Identify the blood parasite species.
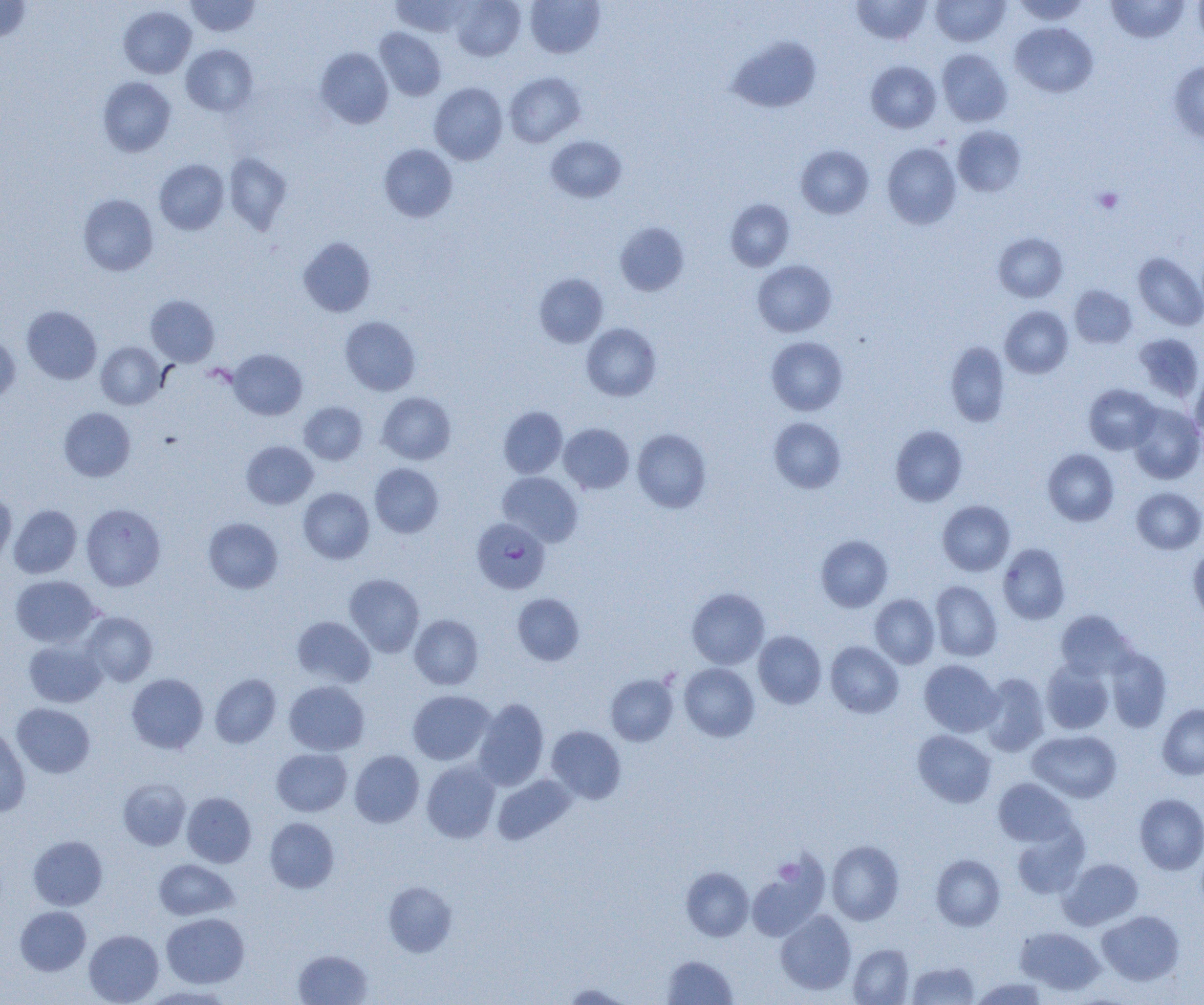
Plasmodium falciparum.

Summary:
  - Coordinate format: approximate bounding boxes as [x1, y1, x2, y2] in pixels
  - Platelet locations: [1093, 187, 1123, 213], [774, 858, 799, 883]
  - Uninfected red blood cell locations: [0, 0, 31, 43], [186, 0, 260, 37], [389, 0, 471, 36], [451, 0, 525, 60], [525, 0, 605, 58], [851, 0, 931, 45], [931, 0, 1009, 46], [1012, 0, 1091, 24], [1106, 0, 1190, 43], [1193, 0, 1204, 49], [119, 6, 196, 78], [1011, 22, 1098, 97], [375, 27, 447, 100], [728, 35, 821, 114], [181, 44, 258, 116], [315, 47, 394, 128], [937, 49, 1012, 126], [1168, 60, 1204, 144], [866, 61, 941, 133], [504, 72, 585, 147], [98, 77, 176, 157], [429, 83, 508, 165], [953, 125, 1026, 197], [545, 135, 626, 203], [882, 143, 961, 229], [379, 144, 458, 222], [795, 145, 874, 218], [224, 152, 292, 234], [154, 159, 229, 235], [78, 194, 158, 275], [725, 199, 794, 271], [615, 222, 689, 296], [993, 232, 1067, 302], [299, 237, 376, 316], [1134, 252, 1204, 330], [752, 260, 836, 337], [534, 273, 608, 347], [1070, 286, 1136, 348], [146, 295, 219, 366], [1000, 305, 1073, 378], [22, 306, 101, 384], [340, 316, 420, 395], [581, 323, 661, 401], [1133, 333, 1204, 402], [0, 334, 20, 403], [766, 336, 848, 415], [96, 341, 167, 409], [945, 341, 1010, 427], [228, 349, 307, 420], [1190, 371, 1204, 444], [1084, 384, 1160, 454], [377, 392, 456, 464], [299, 402, 367, 464], [1128, 402, 1204, 483], [498, 406, 567, 478], [59, 407, 135, 481], [769, 417, 846, 493], [559, 423, 634, 494], [890, 425, 967, 506], [632, 428, 711, 513], [241, 441, 318, 509], [1043, 448, 1118, 525], [370, 463, 443, 537], [498, 472, 583, 546], [298, 487, 374, 563], [1132, 487, 1204, 554], [0, 491, 16, 565], [937, 500, 1015, 575], [81, 503, 166, 591], [8, 504, 81, 578], [203, 517, 283, 594], [815, 535, 893, 612], [997, 543, 1070, 625], [1188, 546, 1204, 624], [344, 574, 424, 656], [11, 575, 101, 647], [930, 581, 1002, 661], [687, 587, 769, 669], [512, 593, 584, 665], [870, 594, 939, 668], [1055, 609, 1135, 680], [81, 612, 157, 686], [409, 614, 483, 689], [291, 616, 375, 688], [753, 631, 826, 708], [23, 638, 106, 707], [826, 641, 903, 717], [1105, 647, 1172, 732], [919, 659, 1002, 737], [1041, 660, 1114, 734], [679, 663, 759, 741], [979, 672, 1049, 756], [126, 673, 208, 754], [210, 674, 281, 748], [605, 674, 678, 746], [284, 681, 369, 755], [408, 690, 494, 765], [473, 698, 549, 790], [12, 703, 95, 778], [1157, 704, 1204, 780], [546, 725, 627, 804], [0, 727, 31, 817], [913, 730, 996, 807], [1028, 730, 1121, 803], [271, 748, 352, 816], [349, 750, 424, 827], [421, 760, 500, 843], [493, 774, 576, 845], [993, 777, 1076, 847], [118, 778, 190, 849], [182, 792, 257, 867], [1134, 793, 1204, 874], [264, 817, 339, 893], [1012, 824, 1089, 899], [28, 835, 108, 910], [827, 840, 904, 925], [931, 854, 1005, 931], [747, 858, 828, 942], [1059, 858, 1142, 929], [154, 859, 238, 920], [681, 866, 754, 941], [384, 881, 456, 957], [15, 906, 91, 976], [776, 910, 856, 995], [1097, 910, 1184, 985], [161, 913, 249, 988], [1016, 926, 1104, 996], [84, 930, 163, 1004], [849, 944, 913, 1004], [293, 949, 372, 1005], [662, 955, 738, 1004], [907, 961, 980, 1005], [971, 977, 1048, 1004], [561, 983, 632, 1004], [142, 985, 235, 1004]
  - Plasmodium falciparum-infected red blood cell locations: [472, 516, 550, 594]
  - Preparation: thin blood film
  - Field of view: single
  - Magnification: 1000x
  - Modality: light microscopy
  - Image size: 1204×1005 pixels